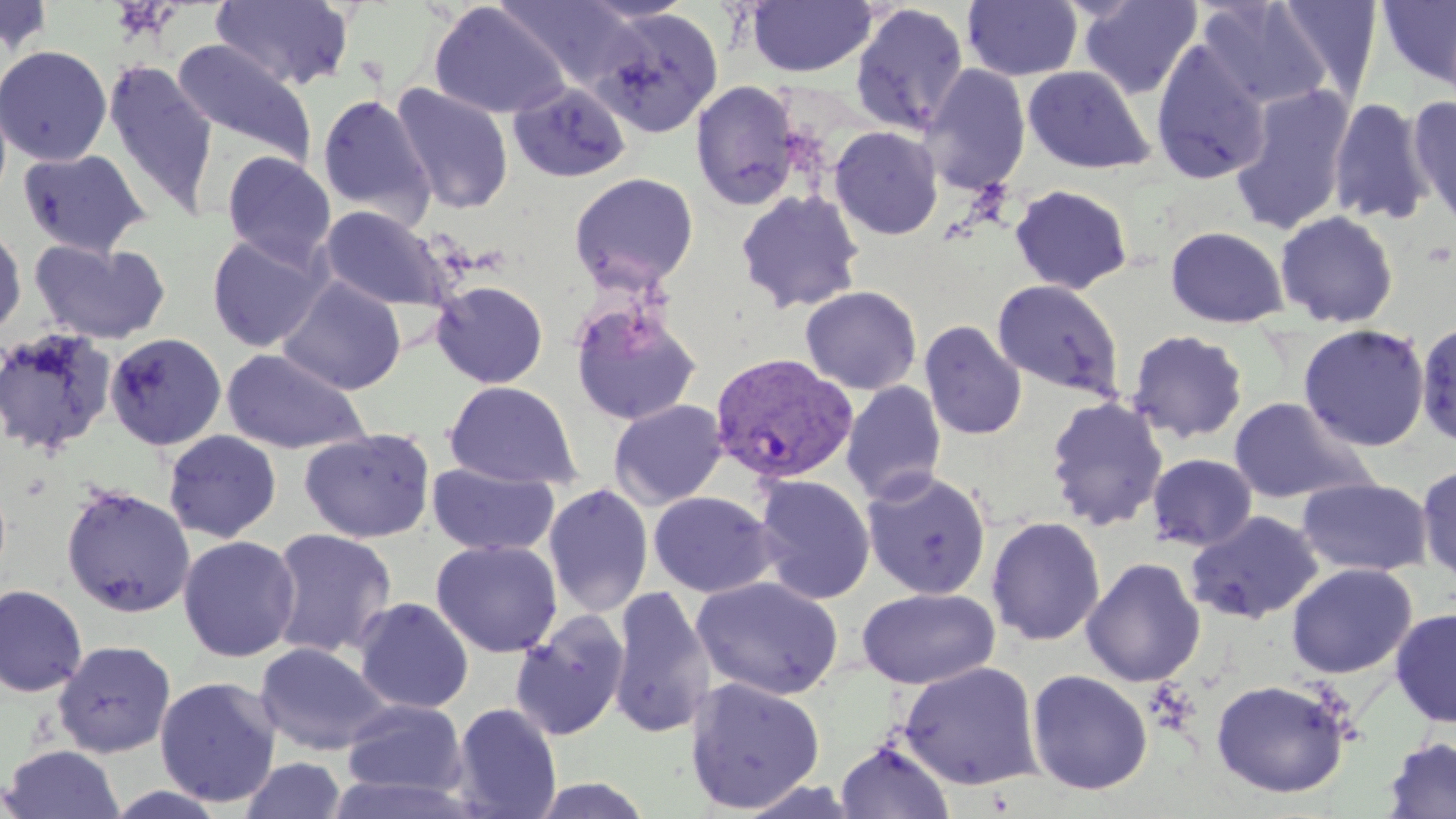

{
  "slide_level_diagnosis": "Plasmodium vivax",
  "preparation": "thin blood film",
  "uninfected_red_blood_cell_locations": "approximate bounding boxes as (x1, y1, x2, y2) in pixels: (211, 0, 355, 92), (496, 0, 643, 92), (963, 0, 1083, 81), (1078, 0, 1202, 99), (1377, 0, 1456, 87), (746, 1, 878, 78), (1197, 1, 1334, 111), (1274, 1, 1383, 102), (429, 2, 571, 119), (849, 2, 970, 137), (587, 6, 724, 139), (172, 39, 317, 167), (1151, 39, 1271, 185), (0, 45, 113, 166), (102, 61, 218, 219), (920, 64, 1031, 196), (1022, 66, 1155, 175), (690, 80, 803, 211), (507, 81, 631, 184), (1230, 82, 1356, 235), (391, 84, 514, 215), (317, 93, 435, 224), (1407, 95, 1456, 227), (1327, 97, 1434, 225), (829, 125, 944, 240), (17, 148, 152, 257), (221, 152, 336, 267), (569, 172, 699, 291), (1009, 184, 1134, 294), (734, 189, 866, 314), (319, 205, 453, 313), (1274, 209, 1399, 328), (0, 224, 27, 339), (1164, 225, 1289, 328), (206, 233, 329, 352), (29, 239, 172, 345), (278, 276, 406, 395), (992, 279, 1125, 400), (431, 280, 549, 388), (800, 285, 922, 395), (569, 299, 703, 428), (1416, 317, 1455, 450), (919, 320, 1027, 441), (1297, 323, 1431, 452), (0, 326, 119, 457), (1126, 329, 1249, 443), (105, 332, 228, 451), (221, 348, 370, 454), (444, 380, 579, 489), (840, 381, 948, 503), (1044, 395, 1169, 531), (1228, 396, 1377, 505), (609, 399, 729, 509), (298, 427, 436, 543), (163, 430, 282, 543), (1146, 452, 1258, 552), (427, 462, 560, 557), (1416, 463, 1456, 586), (861, 469, 992, 600), (752, 474, 876, 604), (1296, 476, 1432, 577), (60, 483, 195, 618), (543, 483, 654, 618), (648, 491, 778, 597), (1185, 510, 1324, 624), (985, 516, 1106, 647), (267, 527, 398, 659), (178, 535, 301, 662), (430, 539, 563, 657), (1081, 557, 1205, 687), (1286, 562, 1417, 679), (691, 576, 844, 700), (0, 584, 87, 698), (608, 585, 716, 738), (856, 587, 1000, 689), (353, 597, 474, 714), (1390, 607, 1456, 727), (510, 612, 629, 741), (52, 639, 176, 758), (254, 642, 391, 756), (897, 660, 1043, 790), (1026, 669, 1153, 795), (155, 676, 281, 807), (684, 676, 826, 814), (1209, 677, 1352, 798), (341, 699, 468, 798), (451, 703, 562, 819), (1381, 736, 1456, 819), (835, 740, 955, 819), (0, 744, 125, 819), (239, 756, 347, 819), (326, 775, 475, 818), (527, 776, 654, 818)",
  "modality": "light microscopy",
  "stain": "May-Grünwald-Giemsa",
  "plasmodium_vivax_infected_red_blood_cell_locations": "approximate bounding boxes as (x1, y1, x2, y2) in pixels: (709, 352, 859, 486)",
  "magnification": "1000x",
  "field_of_view": "single",
  "image_size": "1456×819 pixels"
}